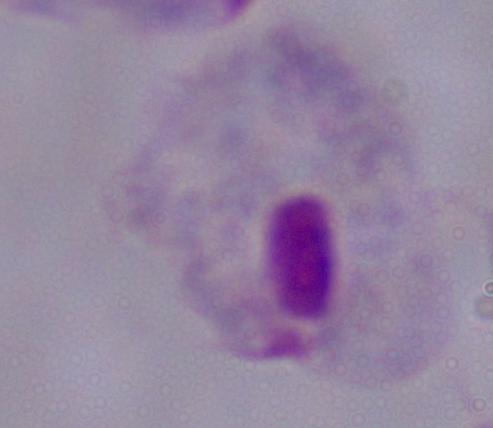
Summary:
  - Modality: photomicrograph
  - Magnification: 1000x
  - Identification: trichomonad